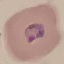
Summary:
  - Result: malaria parasites identified
  - Capture: smartphone through the microscope eyepiece
  - Image type: automatically extracted cell patch, resized to 64 × 64 pixels
  - Preparation: thin smear
  - Stain: Giemsa